Report the malaria status of this cell.
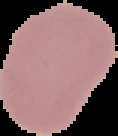
It is uninfected.

preparation: thin blood film
image_size: 118×136 pixels
image_type: cell region segmented out of the field of view; surrounding area masked to black